Describe the morphology of the red blood cells.
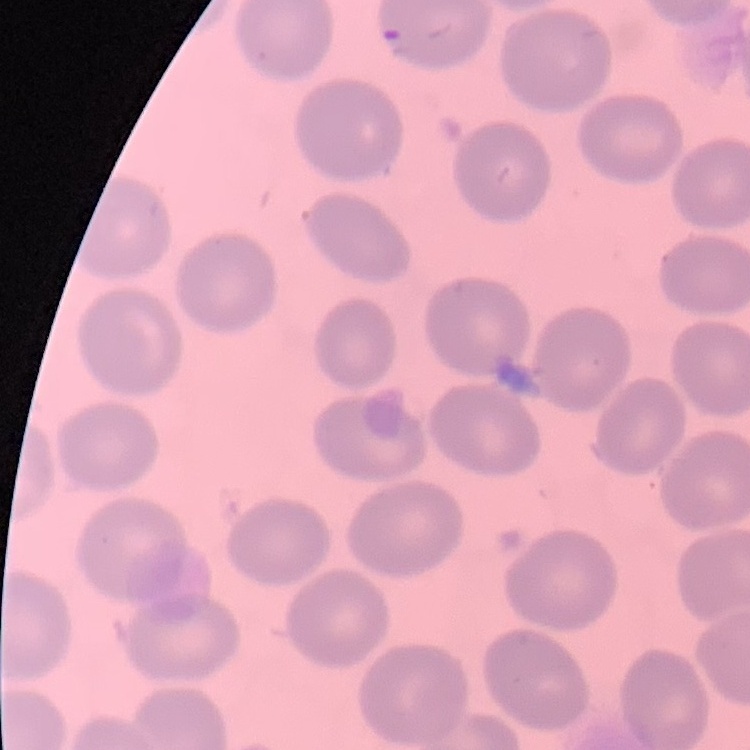

They show no rouleaux formation.

Summary:
  - Preparation: thin blood film
  - Image type: square crop of a larger photomicrograph
  - Stain: Field's or Giemsa